Give the position of every leukocyte visible.
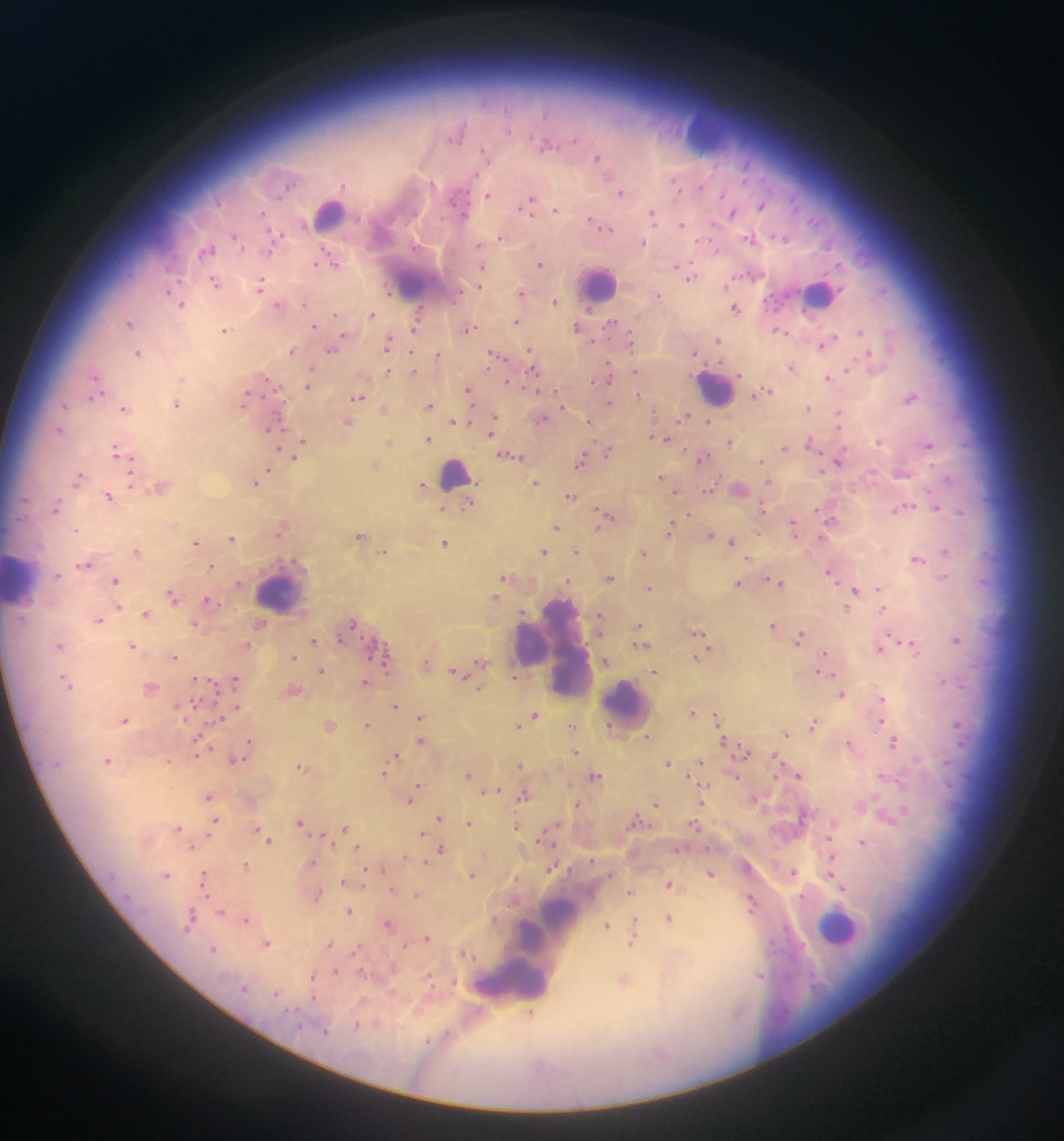
Approximate centers as {x, y} in pixels.
Leukocytes: {710, 129}, {329, 213}, {410, 278}, {598, 284}, {820, 293}, {714, 388}, {454, 474}, {20, 580}, {280, 590}, {552, 646}, {570, 659}, {626, 705}, {837, 926}, {527, 950}, {508, 981}.

Summary:
  - Plasmodium parasite locations: {457, 131}, {546, 143}, {597, 157}, {676, 185}, {620, 191}, {487, 195}, {529, 203}, {761, 204}, {555, 210}, {732, 212}, {652, 214}, {599, 224}, {681, 225}, {234, 236}, {501, 236}, {782, 237}, {751, 239}, {643, 243}, {207, 250}, {332, 261}, {539, 264}, {481, 267}, {691, 276}, {214, 281}, {259, 284}, {479, 285}, {520, 292}, {657, 295}, {554, 300}, {180, 303}, {278, 305}, {735, 308}, {370, 314}, {335, 315}, {516, 321}, {129, 322}, {611, 323}, {314, 326}, {415, 326}, {577, 327}, {469, 328}, {224, 329}, {779, 330}, {860, 332}, {630, 340}, {717, 340}, {340, 341}, {827, 341}, {388, 343}, {332, 348}, {291, 350}, {531, 351}, {694, 352}, {137, 353}, {439, 354}, {497, 355}, {873, 360}, {790, 366}, {532, 369}, {311, 370}, {387, 370}, {413, 371}, {636, 372}, {606, 376}, {830, 378}, {181, 379}, {267, 379}, {94, 381}, {308, 384}, {468, 389}, {762, 392}, {95, 394}, {638, 395}, {358, 397}, {910, 397}, {245, 398}, {610, 402}, {175, 404}, {63, 405}, {429, 405}, {124, 407}, {808, 407}, {383, 409}, {838, 414}, {684, 416}, {540, 419}, {589, 420}, {708, 420}, {347, 421}, {453, 421}, {491, 424}, {270, 427}, {58, 430}, {490, 432}, {662, 438}, {427, 439}, {302, 441}, {388, 441}, {880, 441}, {730, 442}, {812, 442}, {928, 443}, {784, 448}, {607, 450}, {117, 451}, {295, 454}, {510, 455}, {701, 458}, {581, 460}, {837, 463}, {373, 465}, {267, 471}, {902, 471}, {78, 477}, {258, 479}, {663, 479}, {769, 481}, {535, 482}, {160, 485}, {670, 485}, {423, 486}, {737, 489}, {674, 490}, {708, 490}, {108, 496}, {571, 496}, {467, 505}, {55, 507}, {762, 507}, {936, 507}, {442, 508}, {903, 508}, {961, 511}, {606, 516}, {831, 520}, {171, 524}, {281, 526}, {555, 527}, {794, 527}, {670, 528}, {75, 529}, {827, 529}, {360, 535}, {710, 535}, {231, 538}, {731, 541}, {195, 542}, {444, 544}, {576, 550}, {136, 551}, {384, 551}, {544, 551}, {944, 551}, {642, 553}, {917, 559}, {84, 564}, {211, 566}, {830, 572}, {56, 574}, {507, 576}, {608, 577}, {944, 577}, {115, 580}, {777, 582}, {738, 584}, {649, 588}, {880, 588}, {855, 592}, {172, 595}, {495, 597}, {207, 600}, {852, 600}, {117, 608}, {848, 608}, {883, 608}, {146, 614}, {599, 619}, {97, 620}, {258, 624}, {351, 624}, {639, 625}, {773, 625}, {197, 626}, {699, 633}, {800, 637}, {957, 639}, {312, 640}, {640, 643}, {59, 645}, {132, 645}, {246, 645}, {911, 646}, {881, 647}, {825, 655}, {174, 656}, {293, 656}, {698, 656}, {384, 658}, {606, 661}, {480, 663}, {425, 665}, {321, 670}, {822, 671}, {654, 672}, {458, 673}, {514, 677}, {234, 679}, {66, 681}, {365, 681}, {943, 681}, {150, 687}, {479, 689}, {291, 690}, {841, 694}, {881, 698}, {394, 705}, {236, 707}, {692, 712}, {535, 715}, {420, 717}, {219, 718}, {717, 718}, {124, 720}, {527, 721}, {366, 723}, {814, 723}, {957, 723}, {329, 725}, {572, 725}, {518, 726}, {785, 733}, {647, 737}, {198, 739}, {421, 740}, {250, 741}, {724, 741}, {895, 741}, {849, 743}, {743, 750}, {575, 751}, {197, 753}, {395, 756}, {234, 759}, {107, 760}, {167, 760}, {700, 761}, {668, 762}, {301, 765}, {520, 765}, {384, 772}, {798, 774}, {468, 775}, {733, 775}, {594, 777}, {415, 788}, {495, 790}, {488, 792}, {524, 794}, {208, 795}, {410, 798}, {754, 799}, {702, 801}, {655, 803}, {578, 805}, {439, 817}, {892, 817}, {215, 820}, {635, 820}, {299, 822}, {469, 823}, {516, 826}, {177, 827}, {344, 828}, {257, 830}, {423, 833}, {263, 834}, {323, 835}, {545, 835}, {268, 839}, {863, 842}, {192, 846}, {357, 847}, {441, 848}, {405, 858}, {832, 860}, {311, 862}, {245, 865}, {382, 868}, {551, 868}, {793, 872}, {471, 873}, {710, 873}, {167, 874}, {830, 875}, {204, 876}, {364, 876}, {343, 881}, {835, 881}, {669, 884}, {362, 885}, {842, 889}, {392, 890}, {630, 892}, {318, 894}, {416, 894}, {751, 902}, {348, 910}, {221, 911}, {190, 915}, {669, 918}, {246, 919}, {606, 924}, {634, 924}, {389, 925}, {633, 934}, {426, 938}, {631, 942}, {266, 943}, {328, 944}, {213, 949}, {465, 954}, {335, 972}, {760, 975}, {313, 976}, {624, 981}, {276, 993}, {313, 998}, {529, 1014}
  - Preparation: thick blood smear
  - Country: Ghana
  - Field of view: single
  - Capture: mobile-phone photograph through a microscope
  - Image size: 1064×1141 pixels